Locate the Plasmodium falciparum-infected red blood cells and any of indeterminate infection status.
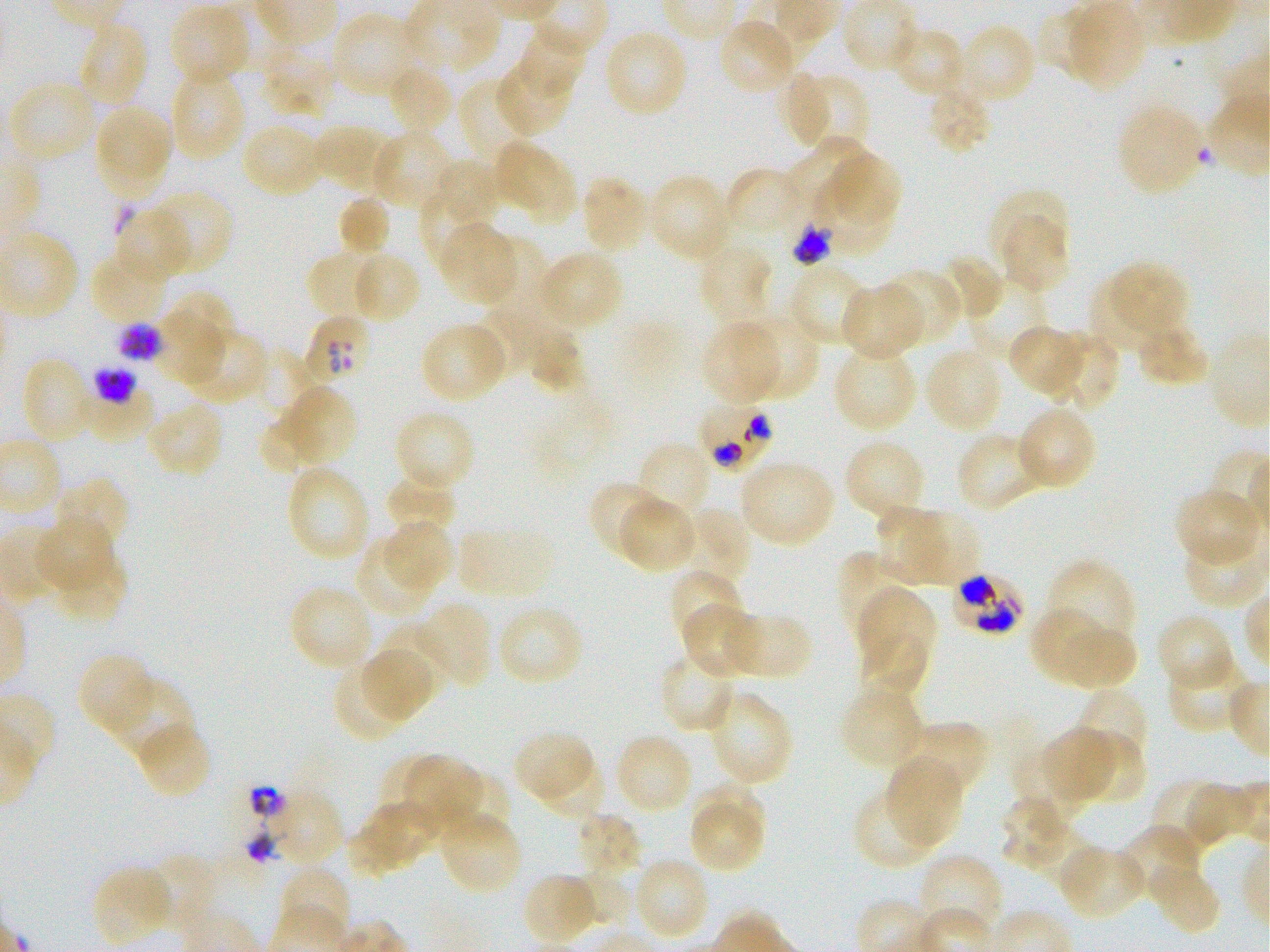

Approximate bounding rectangles given as corner coordinates in pixels from the top-left. Not every red blood cell is marked. A life-cycle stage — or a range of stages, where the recorded stages span more than one — follows each staged infected red blood cell.
Infected red blood cells: (x1=792, y1=222, x2=835, y2=266) late trophozoite to late schizont; (x1=305, y1=315, x2=372, y2=385); (x1=118, y1=323, x2=162, y2=363) late trophozoite to late schizont; (x1=94, y1=365, x2=139, y2=404) late trophozoite to late schizont; (x1=698, y1=401, x2=776, y2=474); (x1=950, y1=573, x2=1026, y2=636).
No red blood cells of indeterminate infection status observed.

locations of uninfected red blood cells = (x1=397, y1=0, x2=497, y2=76), (x1=1067, y1=3, x2=1145, y2=90), (x1=171, y1=4, x2=250, y2=81), (x1=331, y1=11, x2=419, y2=98), (x1=718, y1=18, x2=798, y2=96), (x1=76, y1=22, x2=149, y2=108), (x1=957, y1=22, x2=1037, y2=105), (x1=891, y1=25, x2=967, y2=99), (x1=604, y1=28, x2=689, y2=118), (x1=520, y1=30, x2=588, y2=96), (x1=260, y1=45, x2=338, y2=118), (x1=496, y1=61, x2=572, y2=136), (x1=385, y1=64, x2=454, y2=136), (x1=169, y1=71, x2=246, y2=160), (x1=789, y1=74, x2=830, y2=144), (x1=801, y1=77, x2=866, y2=152), (x1=459, y1=79, x2=536, y2=165), (x1=12, y1=80, x2=96, y2=160), (x1=925, y1=85, x2=992, y2=155), (x1=1117, y1=104, x2=1204, y2=195), (x1=98, y1=110, x2=173, y2=176), (x1=240, y1=123, x2=327, y2=198), (x1=312, y1=123, x2=391, y2=191), (x1=369, y1=130, x2=454, y2=211), (x1=101, y1=137, x2=168, y2=199), (x1=782, y1=137, x2=865, y2=211), (x1=494, y1=142, x2=558, y2=209), (x1=831, y1=152, x2=899, y2=220), (x1=439, y1=160, x2=501, y2=222), (x1=526, y1=161, x2=579, y2=224), (x1=724, y1=167, x2=801, y2=238), (x1=810, y1=170, x2=894, y2=257), (x1=646, y1=172, x2=733, y2=262), (x1=581, y1=176, x2=651, y2=253), (x1=988, y1=187, x2=1070, y2=265), (x1=152, y1=189, x2=232, y2=274), (x1=422, y1=190, x2=492, y2=269), (x1=336, y1=196, x2=391, y2=260), (x1=114, y1=206, x2=191, y2=283), (x1=998, y1=216, x2=1071, y2=293), (x1=439, y1=223, x2=516, y2=304), (x1=488, y1=237, x2=547, y2=318), (x1=698, y1=243, x2=774, y2=327), (x1=538, y1=250, x2=624, y2=329), (x1=88, y1=252, x2=169, y2=325), (x1=939, y1=253, x2=1003, y2=321), (x1=308, y1=254, x2=380, y2=319), (x1=356, y1=256, x2=418, y2=319), (x1=1108, y1=261, x2=1189, y2=337), (x1=789, y1=263, x2=868, y2=346), (x1=879, y1=268, x2=961, y2=346), (x1=965, y1=280, x2=1050, y2=361), (x1=1088, y1=280, x2=1159, y2=354), (x1=838, y1=283, x2=924, y2=361), (x1=171, y1=291, x2=235, y2=349), (x1=479, y1=300, x2=559, y2=372), (x1=152, y1=307, x2=225, y2=385), (x1=738, y1=313, x2=819, y2=401), (x1=700, y1=321, x2=781, y2=405), (x1=1134, y1=322, x2=1210, y2=388), (x1=1007, y1=325, x2=1084, y2=396), (x1=424, y1=327, x2=503, y2=400), (x1=188, y1=330, x2=267, y2=399), (x1=528, y1=332, x2=586, y2=395), (x1=1047, y1=332, x2=1120, y2=411), (x1=831, y1=346, x2=918, y2=431), (x1=257, y1=348, x2=317, y2=414), (x1=924, y1=348, x2=1003, y2=433), (x1=21, y1=356, x2=95, y2=445), (x1=82, y1=382, x2=160, y2=446), (x1=290, y1=386, x2=357, y2=462), (x1=147, y1=400, x2=224, y2=478), (x1=1017, y1=405, x2=1098, y2=491), (x1=258, y1=412, x2=315, y2=474), (x1=401, y1=413, x2=471, y2=485), (x1=955, y1=430, x2=1047, y2=512), (x1=843, y1=439, x2=927, y2=523), (x1=637, y1=440, x2=711, y2=523), (x1=738, y1=459, x2=835, y2=547), (x1=286, y1=464, x2=371, y2=562), (x1=384, y1=473, x2=458, y2=540), (x1=54, y1=476, x2=131, y2=551), (x1=587, y1=480, x2=665, y2=559), (x1=1174, y1=488, x2=1259, y2=566), (x1=616, y1=497, x2=697, y2=572), (x1=875, y1=504, x2=945, y2=582), (x1=681, y1=508, x2=751, y2=586), (x1=903, y1=509, x2=981, y2=585), (x1=34, y1=518, x2=112, y2=594), (x1=382, y1=520, x2=452, y2=593), (x1=1182, y1=534, x2=1267, y2=608), (x1=354, y1=541, x2=432, y2=618), (x1=55, y1=548, x2=127, y2=626), (x1=837, y1=549, x2=911, y2=637), (x1=1046, y1=559, x2=1136, y2=648), (x1=668, y1=568, x2=743, y2=645), (x1=289, y1=585, x2=374, y2=672), (x1=858, y1=586, x2=936, y2=676), (x1=418, y1=602, x2=490, y2=689), (x1=497, y1=603, x2=584, y2=687), (x1=681, y1=603, x2=760, y2=678), (x1=1029, y1=606, x2=1105, y2=685), (x1=727, y1=611, x2=813, y2=680), (x1=1155, y1=614, x2=1236, y2=691), (x1=381, y1=620, x2=452, y2=690), (x1=1059, y1=622, x2=1137, y2=691), (x1=858, y1=631, x2=929, y2=699), (x1=361, y1=646, x2=436, y2=722), (x1=659, y1=651, x2=737, y2=735), (x1=77, y1=652, x2=157, y2=737), (x1=1167, y1=657, x2=1248, y2=734), (x1=333, y1=662, x2=409, y2=743), (x1=105, y1=677, x2=193, y2=762), (x1=839, y1=684, x2=924, y2=771), (x1=1075, y1=688, x2=1149, y2=770), (x1=707, y1=689, x2=794, y2=787), (x1=905, y1=720, x2=989, y2=800), (x1=137, y1=722, x2=213, y2=800), (x1=1041, y1=727, x2=1116, y2=802), (x1=513, y1=731, x2=594, y2=803), (x1=615, y1=733, x2=694, y2=814), (x1=1072, y1=734, x2=1148, y2=805), (x1=1011, y1=748, x2=1081, y2=818), (x1=381, y1=753, x2=453, y2=825), (x1=403, y1=754, x2=481, y2=827), (x1=538, y1=756, x2=604, y2=820), (x1=886, y1=756, x2=963, y2=845), (x1=444, y1=770, x2=512, y2=840), (x1=1150, y1=779, x2=1228, y2=853), (x1=694, y1=782, x2=766, y2=850), (x1=852, y1=788, x2=941, y2=870), (x1=269, y1=789, x2=344, y2=864), (x1=999, y1=796, x2=1073, y2=870), (x1=353, y1=802, x2=431, y2=874), (x1=692, y1=804, x2=765, y2=872), (x1=440, y1=811, x2=523, y2=897), (x1=574, y1=811, x2=644, y2=879), (x1=344, y1=822, x2=410, y2=878), (x1=1119, y1=824, x2=1202, y2=904), (x1=1033, y1=828, x2=1094, y2=888), (x1=1057, y1=845, x2=1145, y2=919), (x1=154, y1=853, x2=214, y2=930), (x1=918, y1=853, x2=1005, y2=936), (x1=633, y1=855, x2=710, y2=942), (x1=1148, y1=860, x2=1221, y2=937), (x1=91, y1=865, x2=173, y2=946), (x1=278, y1=866, x2=352, y2=942), (x1=578, y1=869, x2=631, y2=926), (x1=521, y1=872, x2=599, y2=946)
preparation = thin blood smear
donor blood group = O+
field of view = one from this slide
objective = 100x, oil immersion, numerical aperture 1.25
culture = Plasmodium falciparum strain 3D7, static, in vitro
image size = 1270×952 pixels
stain = Giemsa